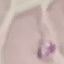
{
  "malaria_status": "parasitized",
  "capture": "smartphone camera at the microscope eyepiece",
  "preparation": "thin smear",
  "image_type": "cell patch, automatically extracted from a larger field of view and resized to 64 × 64 pixels",
  "stain": "Giemsa"
}